Locate every leukocyte (white blood cell).
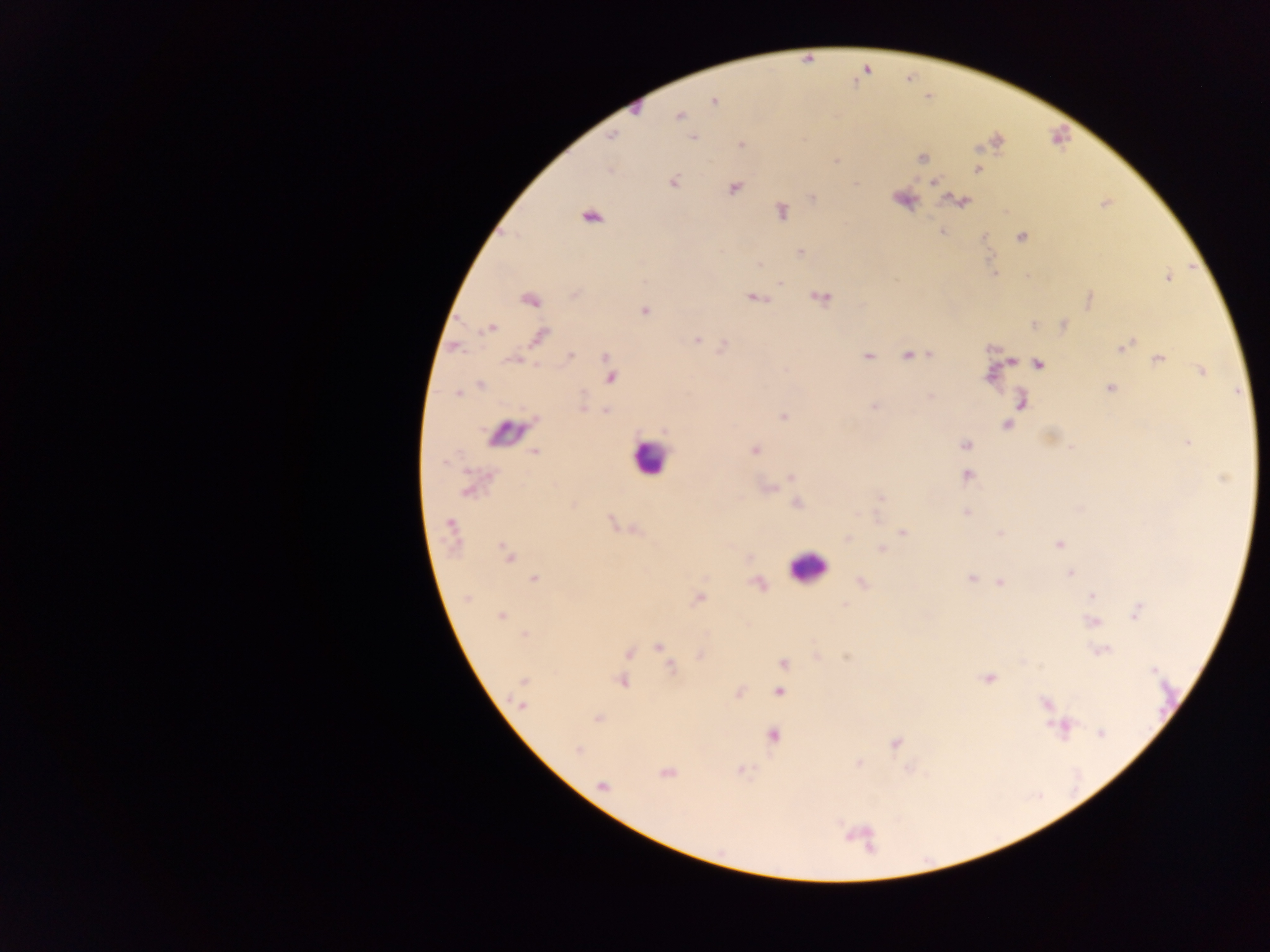

Approximate centers as {x, y} in pixels.
Leukocytes: {649, 457}, {806, 567}.

Summary:
  - Plasmodium parasite locations: {714, 101}, {678, 115}, {611, 136}, {692, 138}, {741, 144}, {922, 158}, {836, 160}, {979, 170}, {673, 182}, {934, 182}, {734, 188}, {812, 198}, {962, 201}, {781, 212}, {591, 217}, {942, 232}, {1021, 237}, {800, 252}, {759, 264}, {1168, 277}, {780, 282}, {755, 298}, {821, 298}, {531, 300}, {645, 310}, {1063, 325}, {1034, 326}, {490, 328}, {539, 335}, {696, 340}, {1124, 345}, {908, 355}, {930, 355}, {869, 356}, {569, 357}, {606, 357}, {1158, 359}, {1038, 365}, {1200, 371}, {611, 378}, {480, 384}, {1110, 389}, {457, 393}, {1022, 402}, {874, 406}, {582, 408}, {607, 411}, {783, 417}, {1007, 424}, {1187, 443}, {965, 445}, {534, 451}, {755, 451}, {967, 476}, {791, 477}, {1224, 478}, {466, 491}, {880, 498}, {797, 503}, {966, 512}, {450, 523}, {903, 532}, {999, 533}, {847, 538}, {1059, 544}, {882, 549}, {507, 553}, {1070, 573}, {535, 579}, {971, 579}, {862, 582}, {1000, 583}, {1091, 596}, {467, 597}, {698, 598}, {1137, 611}, {500, 616}, {1093, 622}, {525, 635}, {659, 647}, {1102, 652}, {784, 663}, {670, 667}, {1153, 670}, {988, 678}, {622, 681}, {524, 682}, {779, 692}, {1045, 703}, {523, 706}, {599, 718}, {1062, 725}, {1101, 733}, {774, 736}, {895, 744}, {578, 750}, {859, 763}, {741, 770}, {665, 773}, {603, 785}
  - Capture: mobile-phone photograph through a microscope
  - Field of view: single
  - Preparation: thick blood smear
  - Image size: 1270×952 pixels
  - Country: Ghana